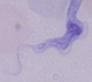 1000x magnification. A trypanosome is seen. Micrograph.